Report the malaria status of this cell.
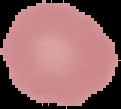
Uninfected.

{
  "preparation": "thin blood smear",
  "image_type": "segmented cell region with the area outside set to black",
  "image_size": "121×109 pixels"
}